Assess this cell for malaria.
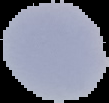

Uninfected.

Summary:
  - Image size: 109×103 pixels
  - Preparation: thin blood smear
  - Image type: segmented cell region with the area outside set to black